Describe the morphology of the red blood cells.
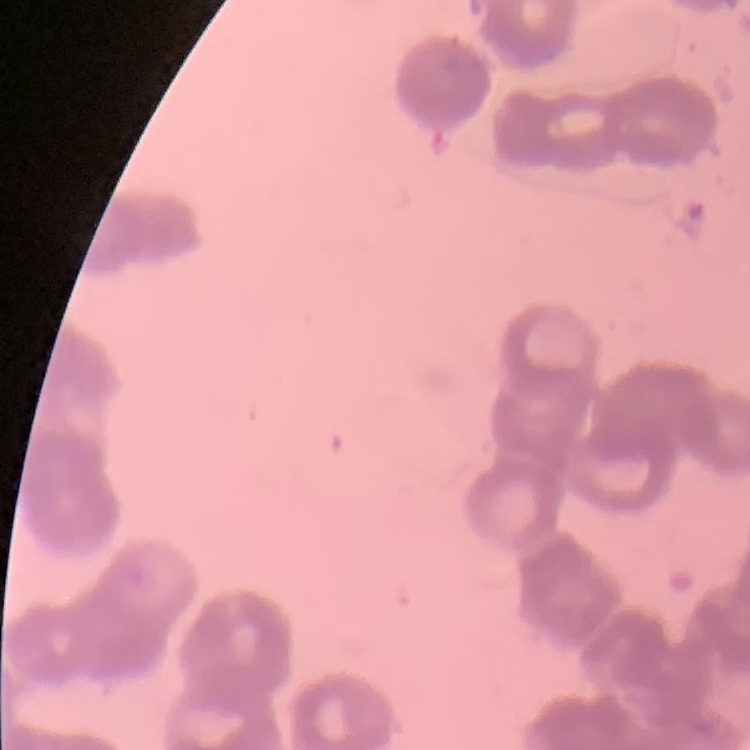

Rouleaux formation.

Summary:
  - Preparation: thin blood film
  - Image type: one tile cut from a larger photomicrograph
  - Stain: Field's or Giemsa